Report the malaria status of this cell.
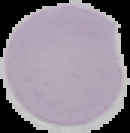

It is uninfected.

image type = segmented cell region on a black background
image size = 130×133 pixels
preparation = thin blood film